State which parasite is depicted.
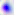
Toxoplasma gondii.

Summary:
  - Magnification: 400x
  - Modality: photomicrograph